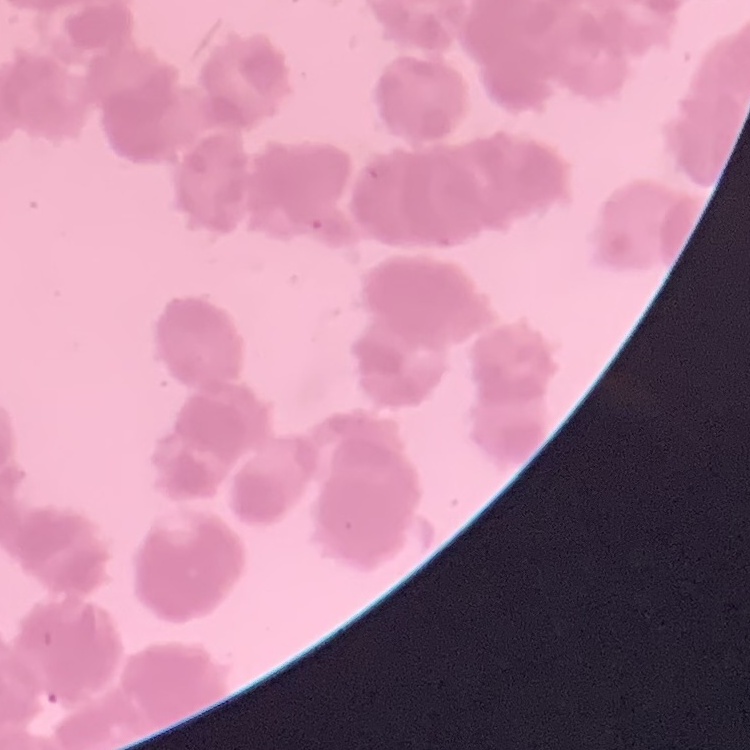
red blood cell morphology = rouleaux formation
image type = square crop of a larger photomicrograph
preparation = thin blood smear
stain = Field's or Giemsa